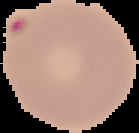 The area outside the segmented cell region is set to black. Malaria status: parasitized. From a thin blood smear. Image is 139×133 pixels.